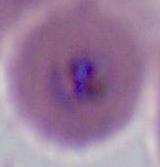
{
  "identification": "Plasmodium",
  "magnification": "400x or 1000x",
  "modality": "photomicrograph"
}